Report the malaria status of this cell.
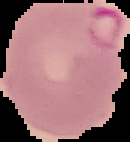
It is parasitized.

Image is 130×142 pixels. Segmented cell region on a black background. From a thin blood smear.